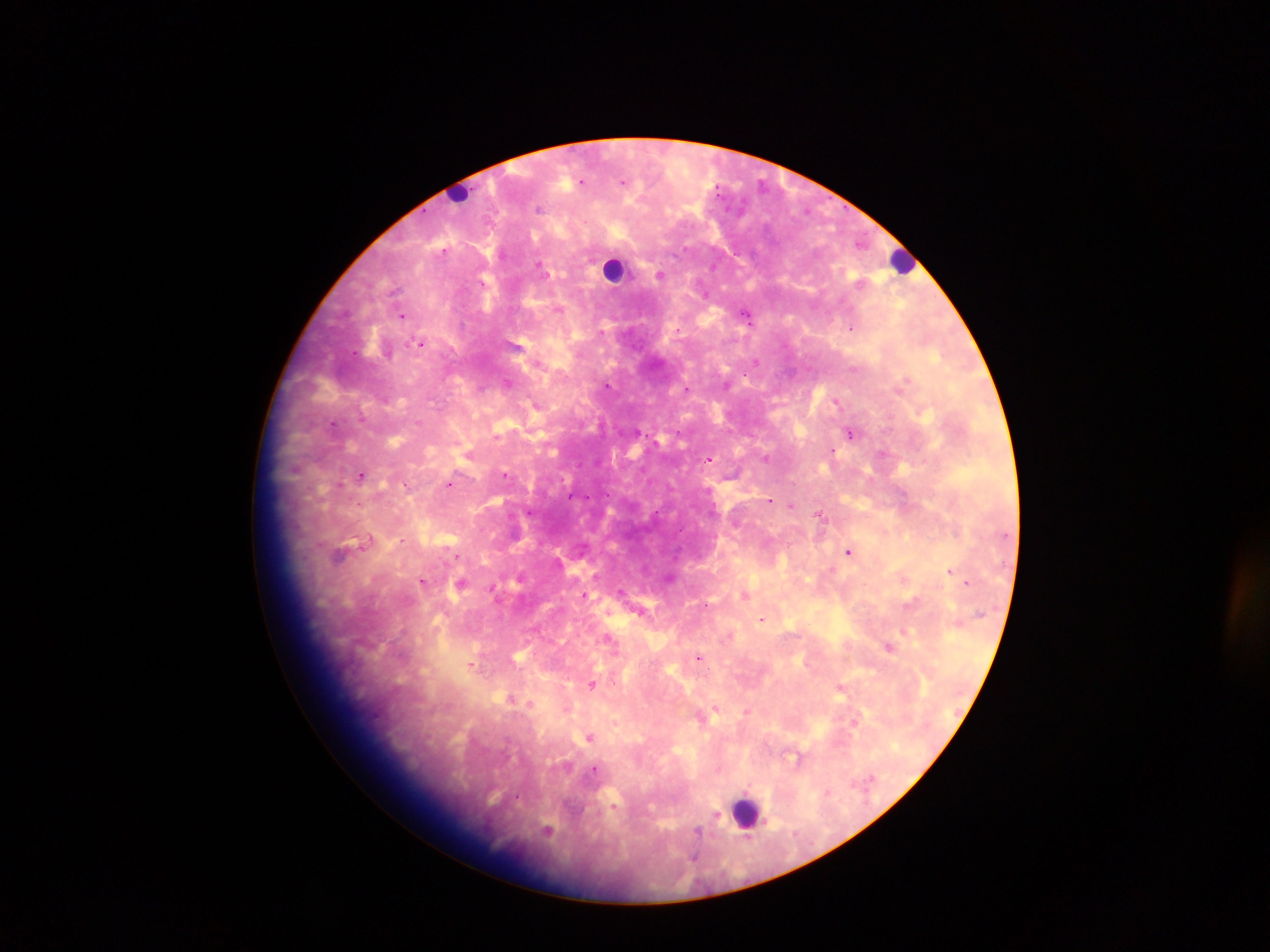

preparation = thick blood film
leukocyte locations = approximate centers as {x, y} in pixels: {462, 193}, {901, 260}, {613, 268}, {747, 812}
image size = 1270×952 pixels
field of view = single
malaria parasite locations = approximate centers as {x, y} in pixels: {582, 181}, {623, 182}, {538, 208}, {860, 244}, {443, 251}, {540, 265}, {660, 274}, {483, 283}, {559, 309}, {747, 314}, {403, 316}, {851, 329}, {601, 332}, {421, 343}, {756, 361}, {507, 382}, {608, 386}, {481, 387}, {687, 388}, {837, 402}, {535, 404}, {363, 417}, {418, 422}, {333, 425}, {850, 432}, {497, 435}, {833, 451}, {882, 454}, {766, 458}, {709, 460}, {362, 475}, {506, 475}, {339, 484}, {449, 484}, {570, 497}, {770, 500}, {790, 506}, {820, 515}, {369, 539}, {402, 540}, {849, 552}, {340, 555}, {457, 555}, {950, 571}, {423, 581}, {967, 582}, {461, 583}, {492, 588}, {621, 591}, {585, 594}, {744, 595}, {760, 619}, {904, 631}, {610, 639}, {889, 648}, {699, 656}, {471, 665}, {593, 684}, {841, 687}, {530, 704}, {715, 708}, {747, 711}, {856, 721}, {589, 737}, {795, 758}, {593, 770}, {715, 816}, {547, 831}, {696, 832}, {696, 849}, {694, 856}
capture = mobile-phone photograph through a microscope
country = Ghana